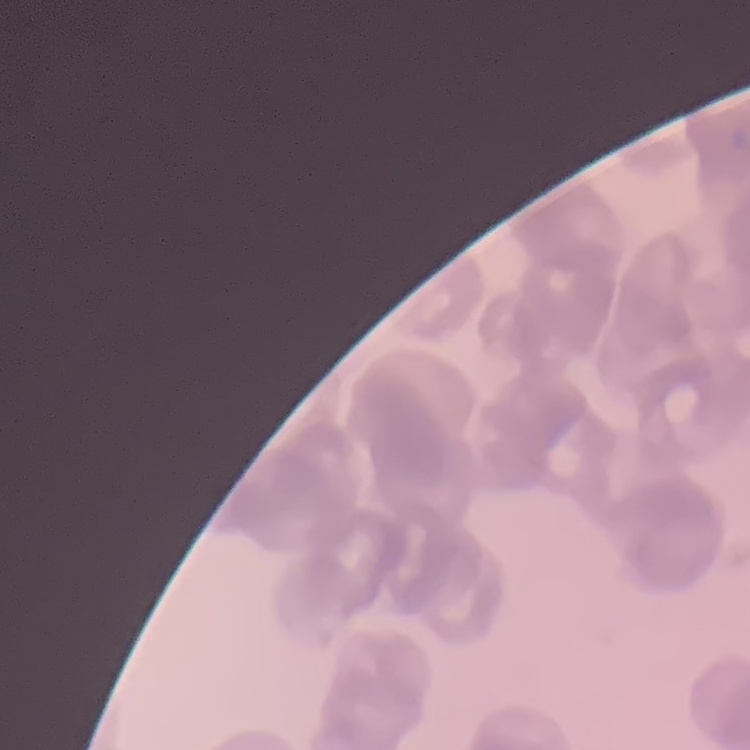
The red blood cells exhibit rouleaux formation. Square crop of a larger photomicrograph. Thin blood film. Stained with either Field's or Giemsa.